Give the preparation type.
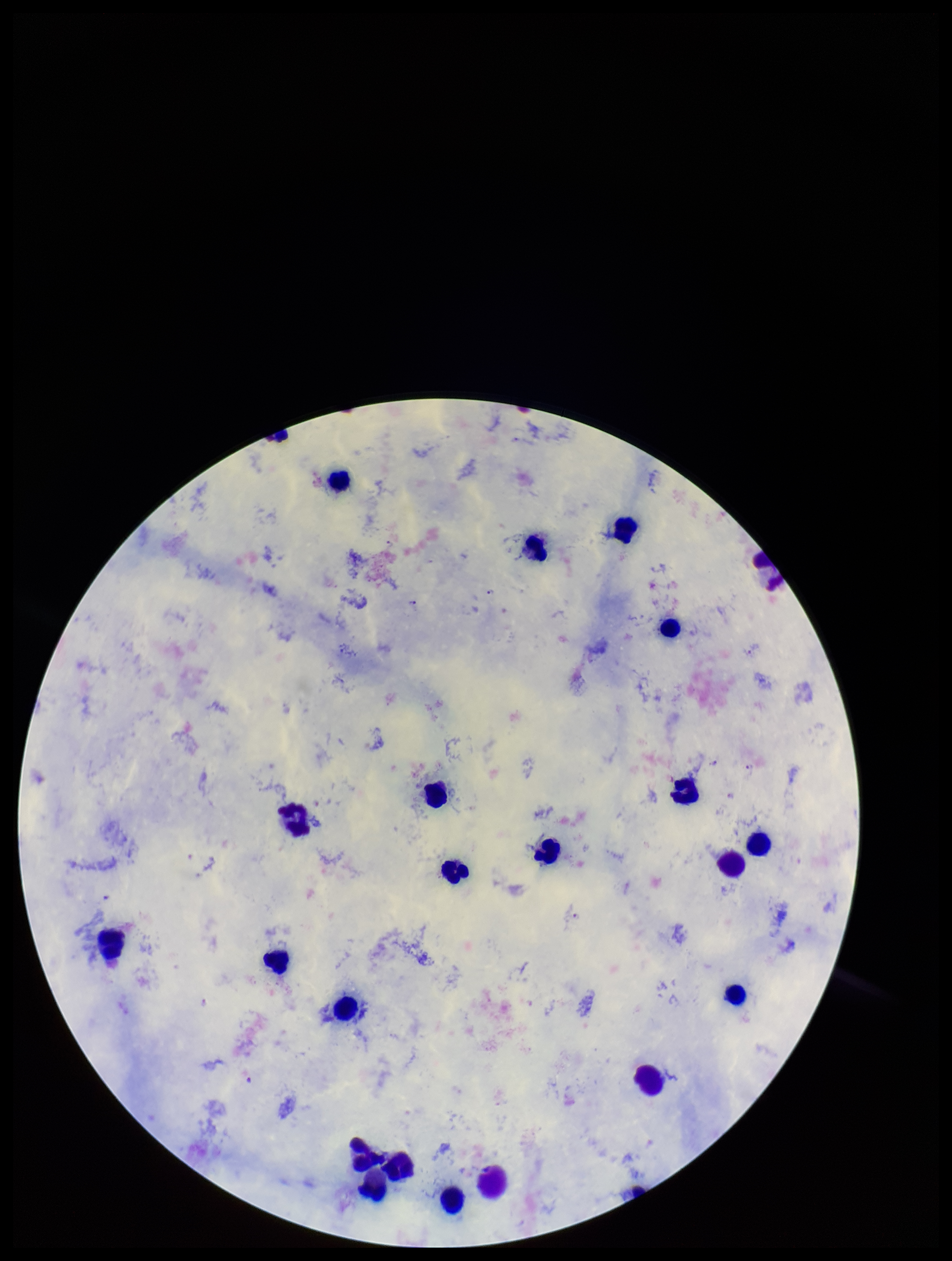

It is a thick blood smear.

Stained with Giemsa. Smartphone photograph taken through the eyepiece of a microscope. Leukocyte count: 21. Plasmodium parasites: seen. Species reported for this patient: Plasmodium falciparum. Parasite count: 10. Image is 952×1261 pixels. Patient malaria status: positive. Single field of view.